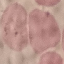 Result: no malaria parasites seen. Automatically extracted cell patch, resized to 64 × 64 pixels. Photographed with a smartphone camera at the microscope eyepiece. Thin blood film. Giemsa-stained preparation.